Give the extent of all uninfected red blood cells.
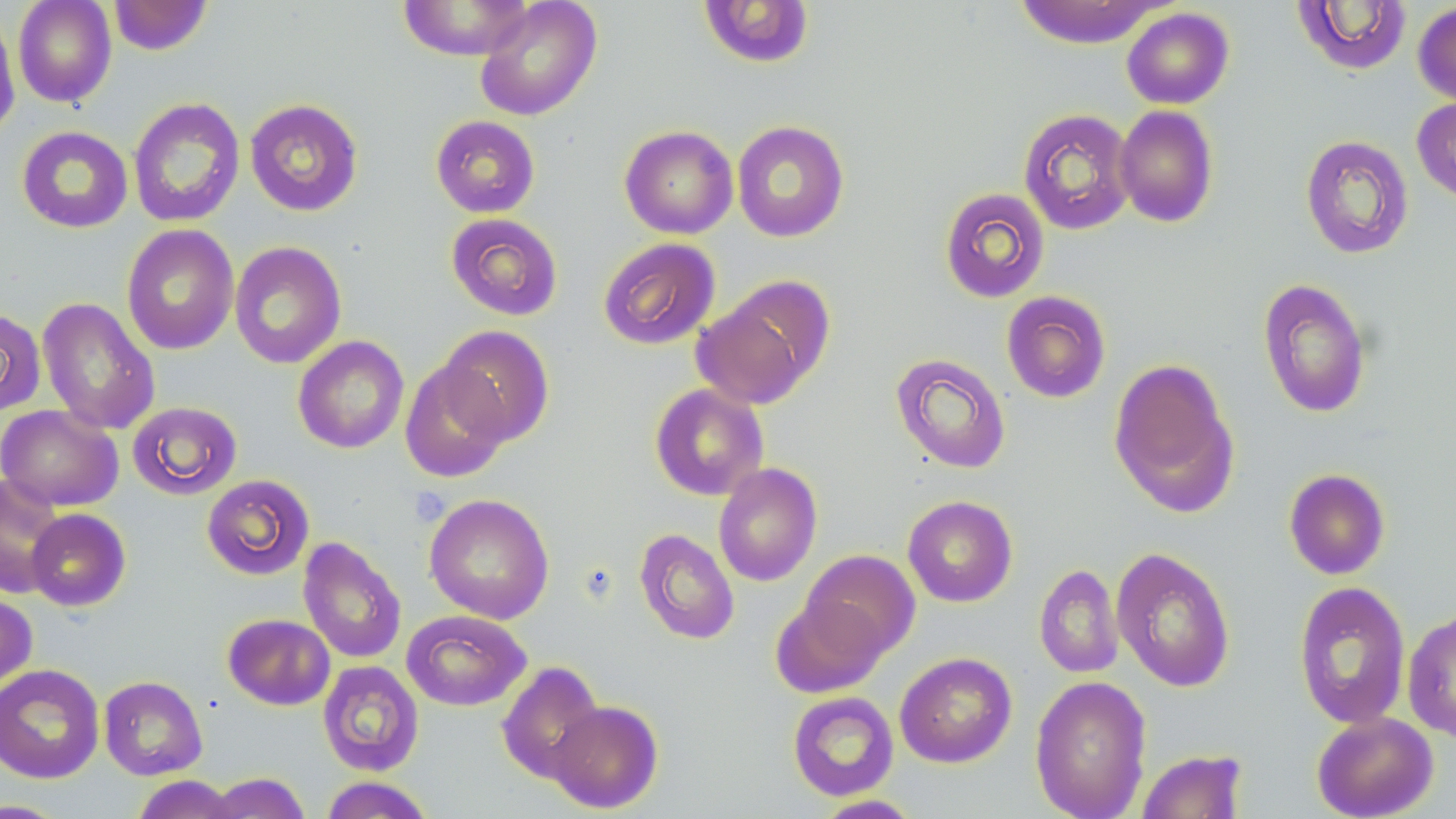
Approximate bounding boxes as named x1/y1/x2/y2 corners in pixels.
Uninfected red blood cells: (x1=12, y1=0, x2=117, y2=108), (x1=108, y1=0, x2=213, y2=55), (x1=474, y1=0, x2=602, y2=121), (x1=1014, y1=0, x2=1169, y2=48), (x1=396, y1=1, x2=538, y2=60), (x1=698, y1=1, x2=815, y2=68), (x1=1291, y1=1, x2=1412, y2=76), (x1=1413, y1=2, x2=1456, y2=107), (x1=1121, y1=7, x2=1235, y2=109), (x1=0, y1=8, x2=20, y2=139), (x1=128, y1=97, x2=246, y2=228), (x1=1412, y1=97, x2=1456, y2=203), (x1=245, y1=98, x2=364, y2=217), (x1=1114, y1=105, x2=1219, y2=228), (x1=1018, y1=108, x2=1136, y2=235), (x1=430, y1=115, x2=540, y2=217), (x1=732, y1=120, x2=849, y2=243), (x1=619, y1=125, x2=738, y2=239), (x1=16, y1=126, x2=133, y2=233), (x1=1299, y1=134, x2=1415, y2=260), (x1=939, y1=187, x2=1050, y2=303), (x1=446, y1=213, x2=563, y2=321), (x1=122, y1=225, x2=239, y2=355), (x1=598, y1=237, x2=721, y2=350), (x1=229, y1=241, x2=347, y2=369), (x1=1257, y1=278, x2=1372, y2=418), (x1=1001, y1=291, x2=1111, y2=403), (x1=692, y1=294, x2=817, y2=409), (x1=37, y1=297, x2=160, y2=435), (x1=0, y1=308, x2=46, y2=414), (x1=437, y1=324, x2=555, y2=445), (x1=292, y1=335, x2=409, y2=454), (x1=891, y1=353, x2=1011, y2=473), (x1=1108, y1=357, x2=1240, y2=517), (x1=399, y1=360, x2=512, y2=483), (x1=649, y1=383, x2=769, y2=501), (x1=127, y1=400, x2=242, y2=500), (x1=0, y1=405, x2=123, y2=511), (x1=713, y1=462, x2=822, y2=587), (x1=1283, y1=468, x2=1391, y2=580), (x1=0, y1=474, x2=67, y2=599), (x1=201, y1=474, x2=315, y2=580), (x1=424, y1=493, x2=555, y2=624), (x1=902, y1=495, x2=1018, y2=607), (x1=26, y1=508, x2=131, y2=611), (x1=634, y1=528, x2=740, y2=645), (x1=298, y1=536, x2=407, y2=664), (x1=1111, y1=546, x2=1236, y2=693), (x1=802, y1=549, x2=920, y2=658), (x1=1034, y1=563, x2=1123, y2=678), (x1=1293, y1=580, x2=1412, y2=729), (x1=0, y1=590, x2=37, y2=693), (x1=771, y1=595, x2=888, y2=698), (x1=1402, y1=608, x2=1456, y2=743), (x1=402, y1=609, x2=531, y2=711), (x1=223, y1=613, x2=336, y2=710), (x1=894, y1=651, x2=1017, y2=768), (x1=317, y1=661, x2=424, y2=776), (x1=496, y1=661, x2=604, y2=784), (x1=0, y1=663, x2=105, y2=784), (x1=99, y1=675, x2=207, y2=780), (x1=1029, y1=675, x2=1152, y2=819), (x1=787, y1=691, x2=899, y2=800), (x1=547, y1=700, x2=663, y2=813), (x1=1311, y1=711, x2=1439, y2=819), (x1=1135, y1=749, x2=1249, y2=819), (x1=205, y1=772, x2=310, y2=818), (x1=132, y1=775, x2=238, y2=819), (x1=319, y1=776, x2=436, y2=818), (x1=812, y1=795, x2=924, y2=818).

{
  "slide_level_diagnosis": "no evidence of blood parasites",
  "preparation": "thin blood smear",
  "magnification": "1000x",
  "field_of_view": "single",
  "platelet_locations": "approximate bounding boxes as named x1/y1/x2/y2 corners in pixels: (x1=411, y1=487, x2=452, y2=524)",
  "image_size": "1456×819 pixels",
  "stain": "May-Grünwald-Giemsa",
  "modality": "light microscopy"
}